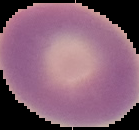

image type = segmented cell region on a black background
malaria status = uninfected
image size = 139×130 pixels
preparation = thin blood smear